Classify this cell by malaria status.
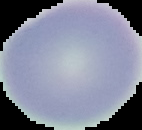

Uninfected.

image type = segmented cell region with the area outside set to black
image size = 142×130 pixels
preparation = thin blood smear